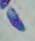

Summary:
  - Identification: Toxoplasma gondii
  - Modality: micrograph
  - Magnification: 1000x